Name the parasite shown.
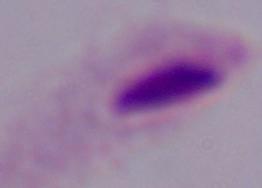

A trichomonad.

modality = photomicrograph
magnification = 1000x